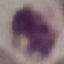

result = negative for malaria parasites
stain = Giemsa
image type = cell patch, automatically extracted from a larger field of view and resized to 64 × 64 pixels
preparation = thin blood film
capture = smartphone camera at the microscope eyepiece